Locate every Trypanosoma brucei.
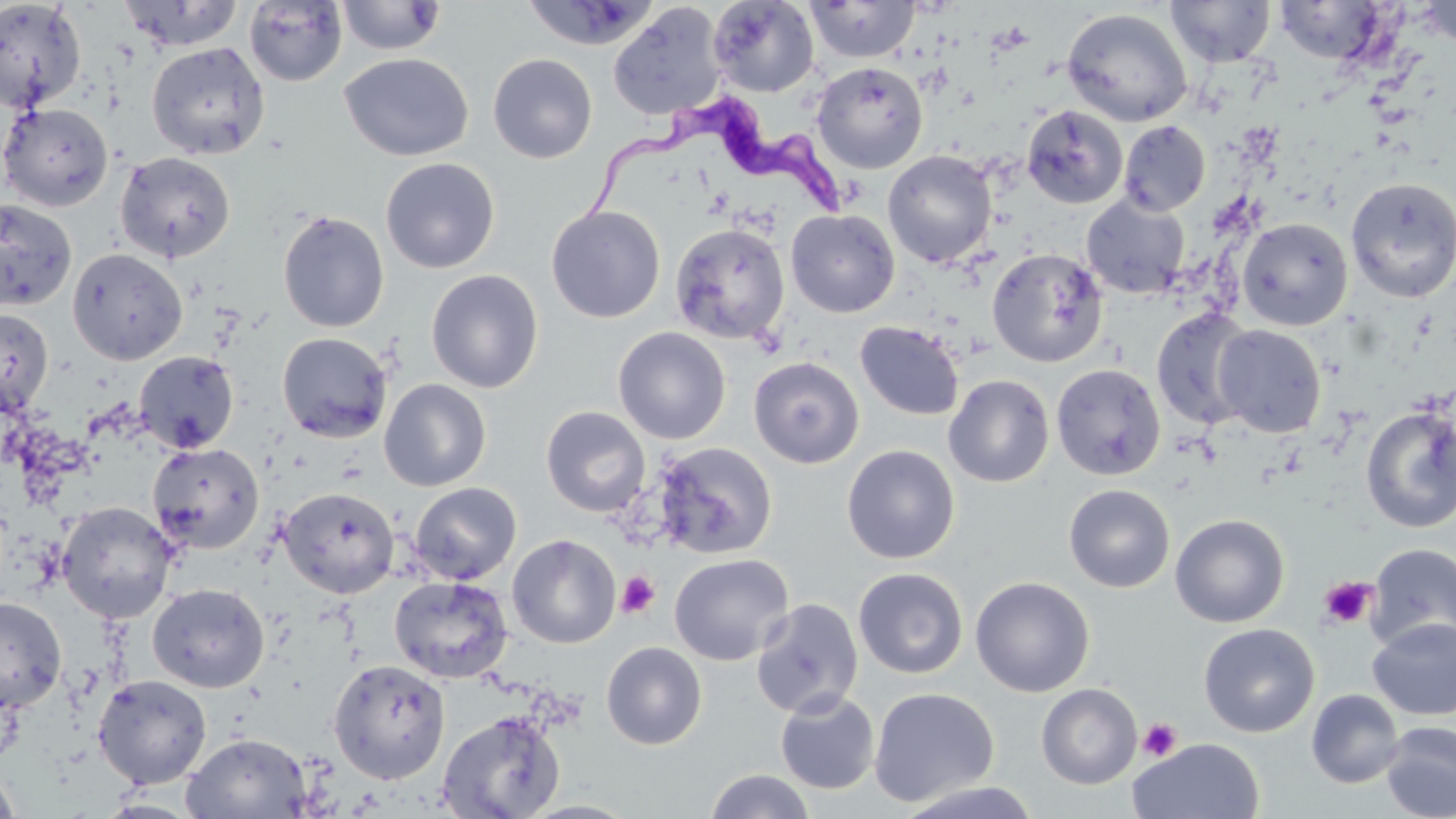

Approximate bounding boxes as (x1, y1, x2, y2) in pixels.
Trypanosoma brucei: (575, 94, 855, 230).

Platelet locations: (615, 571, 660, 619), (1318, 576, 1378, 629), (1137, 717, 1182, 762). Uninfected red blood cell locations: (0, 0, 87, 114), (118, 0, 244, 51), (522, 0, 663, 51), (707, 0, 819, 97), (1165, 0, 1277, 67), (1273, 0, 1390, 65), (243, 1, 347, 87), (334, 1, 448, 55), (805, 1, 919, 63), (1415, 1, 1456, 47), (607, 3, 728, 121), (1061, 7, 1193, 126), (146, 41, 270, 160), (340, 52, 473, 161), (488, 53, 598, 163), (812, 61, 928, 173), (0, 102, 114, 211), (1021, 105, 1128, 209), (1117, 120, 1210, 216), (882, 150, 997, 268), (115, 151, 236, 263), (380, 157, 501, 273), (1345, 177, 1456, 303), (1081, 194, 1190, 300), (0, 199, 77, 311), (546, 205, 665, 322), (786, 209, 900, 317), (277, 210, 390, 333), (1236, 217, 1353, 331), (670, 223, 790, 345), (67, 248, 188, 365), (987, 248, 1108, 368), (426, 269, 544, 393), (0, 307, 54, 417), (1150, 307, 1256, 429), (855, 320, 965, 420), (1212, 324, 1326, 438), (612, 326, 731, 444), (276, 332, 393, 443), (134, 351, 240, 453), (749, 356, 864, 468), (1051, 364, 1166, 480), (943, 374, 1054, 487), (379, 379, 491, 491), (1360, 405, 1456, 533), (541, 406, 651, 517), (148, 442, 264, 554), (652, 442, 778, 559), (842, 444, 960, 564), (410, 482, 522, 585), (1063, 484, 1175, 593), (278, 487, 399, 599), (56, 502, 178, 623), (1170, 513, 1290, 628), (507, 534, 622, 648), (1367, 543, 1456, 652), (669, 554, 794, 665), (853, 567, 969, 679), (389, 576, 513, 684), (970, 576, 1095, 697), (148, 583, 270, 693), (0, 596, 67, 711), (750, 598, 863, 718), (1366, 618, 1456, 720), (1198, 623, 1319, 737), (601, 641, 707, 750), (328, 659, 450, 783), (92, 674, 212, 789), (1036, 683, 1142, 789), (868, 687, 999, 807), (1306, 689, 1405, 788), (774, 690, 880, 794), (437, 710, 566, 819), (1380, 722, 1456, 819), (182, 732, 312, 818), (1128, 738, 1266, 819), (0, 766, 21, 819), (705, 769, 816, 819), (894, 780, 1046, 818), (517, 800, 641, 818). Slide-level diagnosis: Trypanosoma brucei. Image is 1456×819 pixels. Thin blood film. One field of a larger specimen. May-Grünwald-Giemsa stain. Captured at 1000x magnification. Optical microscopy.